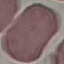

result: negative for malaria parasites
stain: Giemsa
capture: smartphone through the microscope eyepiece
image_type: automatically extracted cell patch, resized to 64 × 64 pixels
preparation: thin blood film